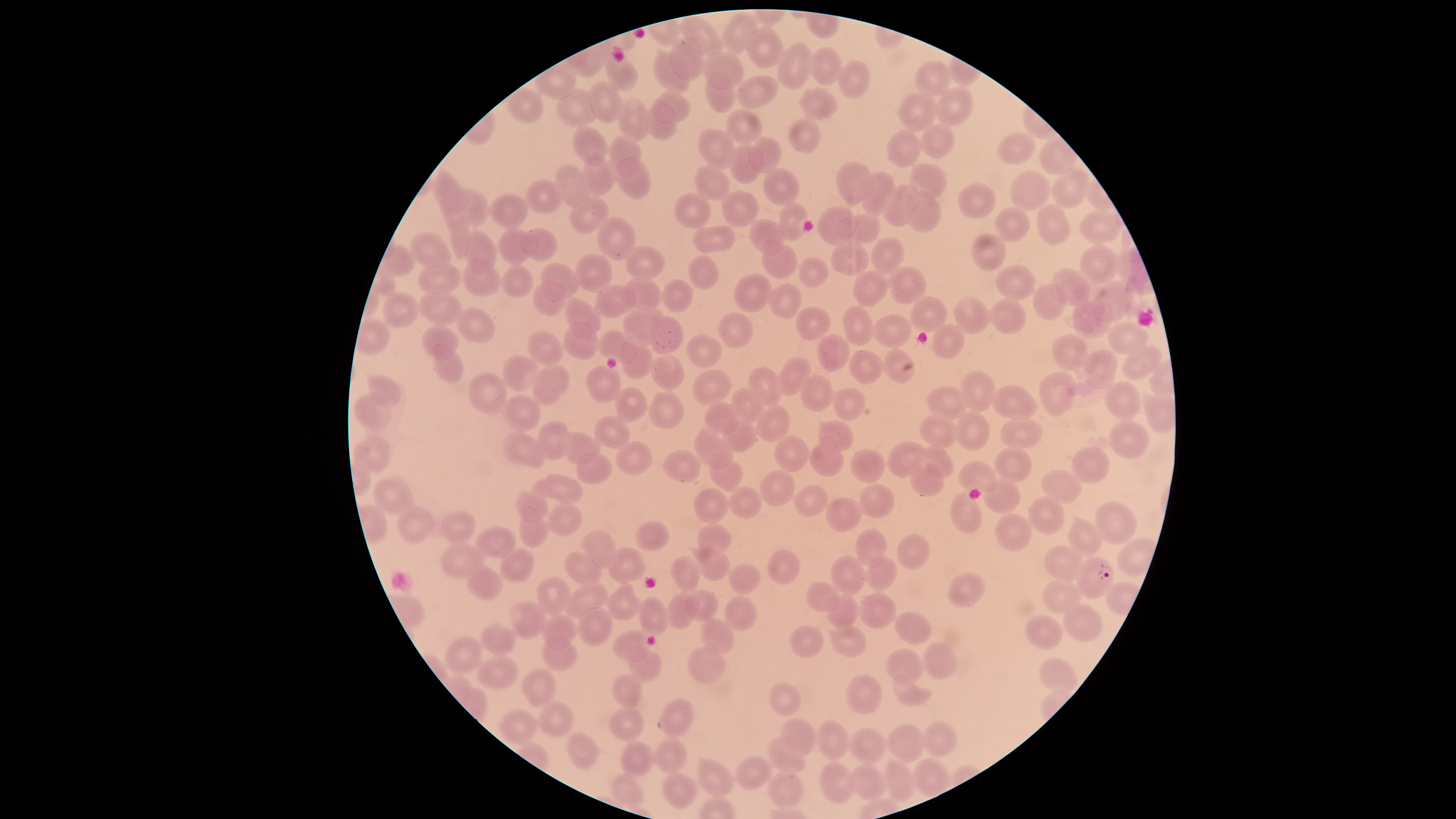

Approximate bounding boxes as [left, top, right, bottom] in pixels.
Summary:
  - Uninfected RBCs: [721, 11, 757, 55], [680, 16, 724, 58], [744, 26, 784, 69], [669, 37, 703, 82], [777, 42, 813, 90], [811, 48, 842, 87], [604, 51, 638, 92], [653, 51, 690, 95], [700, 52, 744, 90], [839, 60, 872, 99], [914, 60, 952, 96], [705, 70, 736, 114], [736, 74, 778, 109], [587, 80, 622, 123], [934, 87, 973, 128], [799, 88, 839, 121], [556, 89, 599, 127], [654, 90, 691, 123], [897, 92, 937, 132], [617, 97, 651, 143], [646, 100, 677, 140], [725, 109, 761, 146], [789, 116, 820, 153], [570, 124, 607, 167], [920, 124, 955, 159], [696, 128, 735, 170], [886, 128, 922, 167], [997, 131, 1035, 165], [608, 135, 641, 177], [748, 136, 782, 174], [729, 143, 763, 183], [581, 152, 615, 197], [615, 158, 650, 200], [834, 161, 873, 205], [909, 162, 947, 199], [555, 164, 592, 209], [694, 165, 730, 202], [1051, 167, 1089, 209], [763, 168, 800, 206], [862, 170, 895, 217], [432, 171, 468, 215], [1010, 171, 1050, 211], [525, 180, 565, 214], [958, 182, 995, 219], [883, 184, 919, 226], [456, 187, 490, 227], [720, 189, 759, 229], [906, 191, 940, 233], [488, 193, 530, 229], [673, 193, 711, 229], [568, 197, 609, 234], [439, 198, 470, 259], [779, 201, 807, 241], [1037, 203, 1071, 245], [994, 206, 1030, 242], [817, 207, 859, 245], [1080, 211, 1121, 244], [836, 214, 881, 244], [597, 216, 636, 261], [749, 219, 785, 255], [693, 226, 737, 253], [497, 227, 539, 265], [521, 228, 557, 261], [465, 229, 497, 275], [410, 231, 451, 271], [971, 233, 1006, 271], [871, 237, 905, 275], [761, 241, 799, 278], [830, 241, 870, 276], [1079, 244, 1119, 285], [625, 246, 665, 280], [574, 253, 612, 293], [689, 255, 719, 289], [461, 257, 502, 298], [799, 257, 829, 287], [541, 263, 578, 303], [417, 264, 461, 295], [995, 264, 1036, 300], [502, 265, 533, 298], [888, 266, 926, 305], [1049, 268, 1091, 308], [852, 269, 888, 308], [734, 273, 772, 313], [620, 278, 663, 311], [663, 279, 694, 313], [1092, 280, 1135, 323], [532, 281, 565, 318], [1033, 282, 1067, 321], [769, 283, 801, 318], [594, 285, 638, 318], [418, 291, 463, 326], [383, 292, 418, 329], [909, 296, 948, 333], [564, 297, 602, 339], [954, 297, 990, 335], [988, 298, 1026, 335], [1072, 301, 1113, 340], [623, 303, 666, 346], [795, 306, 830, 340], [842, 306, 873, 346], [456, 308, 495, 343], [718, 312, 753, 350], [873, 314, 910, 348], [651, 316, 684, 354], [563, 322, 598, 360], [1106, 322, 1149, 356], [931, 323, 965, 360], [421, 325, 459, 360], [596, 330, 636, 364], [527, 332, 563, 367], [1052, 333, 1090, 371], [816, 334, 850, 372], [686, 335, 721, 368], [621, 342, 653, 380], [432, 344, 464, 384], [1122, 345, 1162, 381], [883, 348, 915, 384], [849, 349, 883, 385], [1083, 350, 1117, 389], [650, 355, 684, 391], [502, 356, 539, 393], [777, 357, 811, 396], [532, 364, 569, 405], [586, 365, 621, 403], [748, 367, 782, 408], [692, 369, 732, 404], [961, 370, 995, 413], [1039, 371, 1076, 416], [467, 372, 507, 415], [367, 374, 401, 408], [800, 374, 833, 412], [1104, 382, 1142, 421], [991, 385, 1038, 420], [926, 386, 968, 420], [615, 387, 648, 424], [831, 387, 866, 421], [731, 388, 764, 424], [648, 391, 684, 430], [354, 392, 390, 432], [503, 394, 541, 432], [704, 402, 738, 435], [755, 404, 791, 443], [955, 412, 990, 451], [920, 414, 959, 448], [595, 415, 629, 449], [999, 419, 1042, 449], [538, 420, 569, 461], [719, 420, 758, 452], [818, 420, 853, 452], [1109, 420, 1149, 460], [694, 430, 733, 469], [503, 431, 546, 468], [557, 431, 600, 465], [353, 436, 390, 473], [774, 436, 810, 472], [809, 437, 844, 477], [615, 441, 653, 475], [887, 441, 925, 477], [921, 445, 955, 479], [993, 446, 1031, 483], [1069, 446, 1110, 483], [850, 449, 885, 484], [663, 451, 702, 483], [576, 453, 613, 485], [708, 453, 742, 491], [958, 460, 996, 494], [910, 463, 944, 497], [758, 470, 796, 507], [1041, 471, 1081, 504], [532, 473, 583, 502], [373, 478, 412, 515], [983, 478, 1020, 514], [794, 483, 829, 516], [857, 484, 894, 519], [728, 486, 762, 520], [514, 489, 550, 522], [693, 489, 729, 524], [950, 493, 983, 533], [1029, 496, 1064, 534], [826, 498, 863, 531], [1095, 501, 1136, 546], [546, 503, 584, 537], [397, 506, 433, 544], [519, 506, 549, 549], [439, 511, 476, 546], [993, 512, 1032, 551], [1067, 518, 1101, 557], [635, 521, 670, 550], [696, 524, 731, 557], [475, 527, 516, 558], [855, 528, 887, 568], [581, 530, 616, 570], [897, 533, 932, 569], [440, 543, 486, 581], [693, 546, 729, 581], [1043, 546, 1085, 582], [499, 547, 533, 582], [608, 547, 645, 583], [766, 550, 801, 584], [562, 552, 601, 587], [865, 554, 897, 592], [670, 556, 701, 593], [830, 556, 865, 596], [728, 562, 761, 594], [465, 563, 502, 601], [948, 573, 986, 609], [537, 577, 571, 618], [1042, 580, 1082, 613], [606, 581, 641, 620], [805, 581, 839, 612], [566, 582, 607, 619], [685, 589, 718, 621], [666, 592, 699, 630], [858, 592, 896, 628], [824, 594, 857, 630], [724, 596, 757, 631], [638, 597, 668, 636], [507, 601, 547, 640], [1061, 604, 1102, 643], [578, 607, 613, 648], [894, 611, 932, 645], [541, 615, 578, 650], [1025, 615, 1064, 650], [700, 618, 735, 655], [479, 623, 515, 656], [789, 624, 824, 659], [829, 627, 867, 658], [613, 630, 652, 663], [444, 636, 483, 676], [542, 636, 577, 672], [922, 643, 957, 680], [688, 646, 726, 684], [886, 647, 923, 686], [627, 648, 663, 683], [476, 654, 519, 689], [1039, 658, 1076, 693], [521, 668, 556, 707], [891, 672, 932, 707], [612, 674, 643, 709], [846, 674, 883, 714], [768, 682, 802, 716], [659, 698, 693, 737], [537, 700, 574, 737], [608, 706, 643, 742], [499, 709, 536, 745], [780, 718, 817, 757], [817, 720, 849, 761], [921, 721, 958, 758], [887, 723, 923, 764], [849, 727, 885, 764], [567, 731, 599, 771], [653, 736, 687, 774], [767, 736, 804, 773], [619, 739, 654, 777], [736, 756, 771, 791], [697, 758, 733, 798], [885, 759, 914, 801], [819, 761, 854, 804], [851, 762, 887, 800], [769, 770, 804, 811], [663, 771, 697, 809], [612, 773, 643, 809]
  - Parasitized RBCs: [1075, 557, 1112, 599]
  - Image size: 1456×819 pixels
  - Capture: smartphone photograph through the microscope eyepiece
  - Presence: malaria parasites identified
  - Species: Plasmodium falciparum
  - Visible region: circular
  - Field of view: single
  - Preparation: thin blood smear
  - Stain: Giemsa